Outline each Plasmodium falciparum-infected red blood cell.
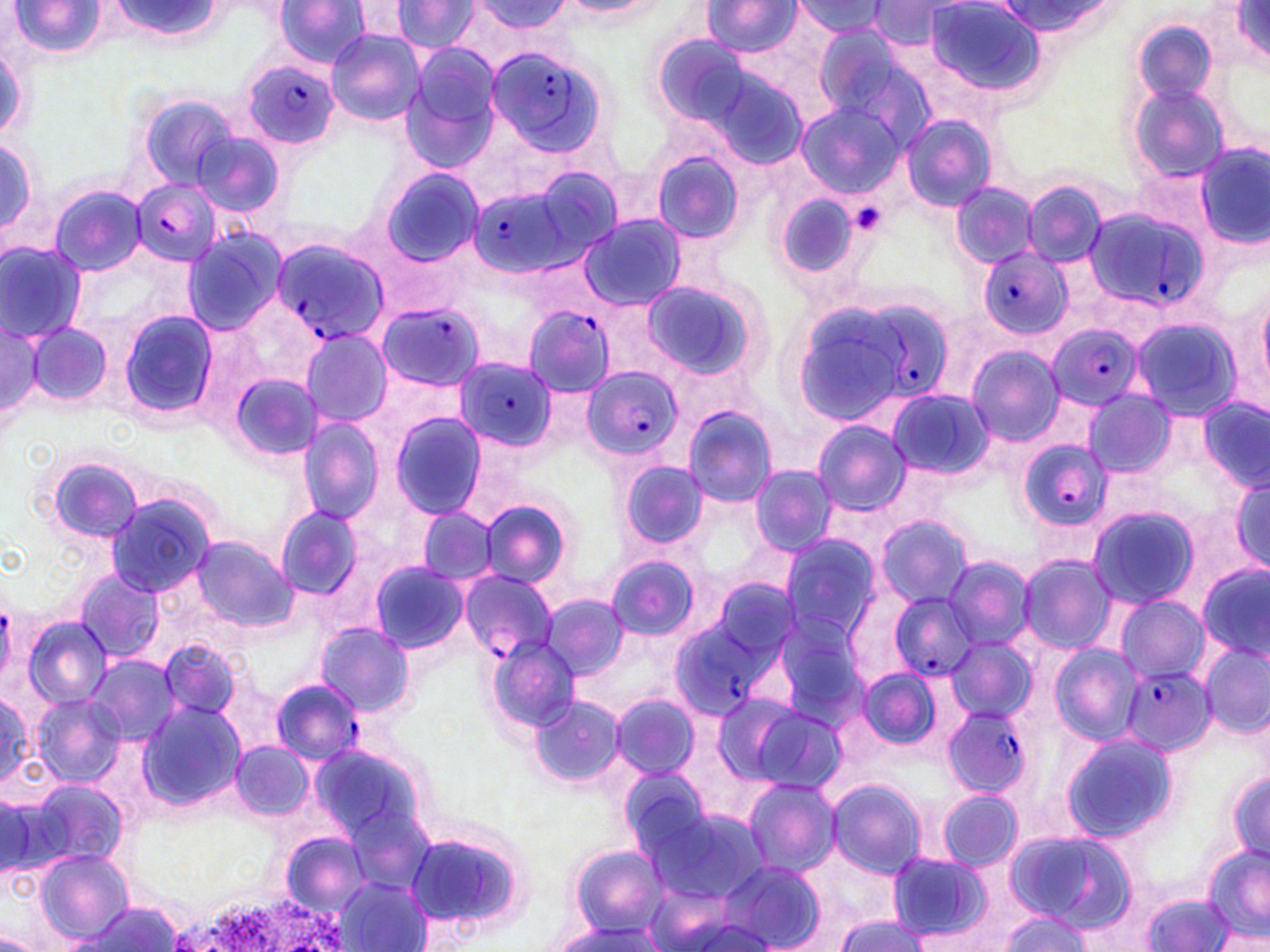

Approximate bounding boxes as (x1,y1)-(x2,y2) corner pairs in pixels.
Plasmodium falciparum-infected red blood cells: (483,40)-(618,158), (244,61)-(341,149), (131,180)-(221,265), (466,180)-(590,281), (1077,206)-(1210,317), (270,238)-(390,345), (979,248)-(1072,335), (853,296)-(949,397), (378,301)-(488,389), (523,306)-(616,395), (1044,323)-(1143,412), (455,357)-(557,451), (581,366)-(681,461), (1015,436)-(1107,537), (458,568)-(558,662), (887,591)-(982,681), (666,602)-(793,722), (1122,667)-(1215,754), (271,677)-(365,765), (944,705)-(1033,797).

Summary:
  - Uninfected red blood cell locations: (7,0)-(107,59), (273,1)-(374,68), (351,1)-(417,46), (391,1)-(483,55), (465,1)-(577,42), (558,1)-(667,21), (702,2)-(802,55), (792,2)-(892,38), (867,2)-(958,48), (924,2)-(1047,95), (1226,2)-(1270,67), (105,3)-(228,43), (987,3)-(1125,38), (1132,20)-(1219,109), (815,26)-(932,141), (324,28)-(424,125), (1,39)-(31,143), (401,46)-(503,170), (1126,81)-(1231,182), (134,93)-(242,191), (794,102)-(902,200), (901,114)-(996,213), (189,129)-(286,218), (0,134)-(43,251), (1191,146)-(1269,250), (648,150)-(748,244), (374,167)-(484,269), (950,182)-(1039,267), (1022,182)-(1108,268), (48,184)-(149,275), (774,192)-(864,282), (579,214)-(690,312), (180,227)-(288,336), (0,241)-(89,343), (639,276)-(770,384), (1256,281)-(1270,402), (117,309)-(219,421), (1127,315)-(1243,421), (1,318)-(43,427), (25,320)-(113,411), (298,328)-(392,427), (965,345)-(1064,447), (228,373)-(323,462), (886,387)-(993,480), (1082,391)-(1175,476), (1198,397)-(1269,491), (682,405)-(778,508), (387,411)-(488,520), (299,419)-(384,522), (812,420)-(911,517), (38,452)-(150,549), (619,459)-(710,549), (748,464)-(838,555), (1225,471)-(1270,579), (106,494)-(216,597), (475,497)-(576,593), (273,504)-(366,601), (1086,504)-(1202,609), (417,507)-(500,585), (875,515)-(975,609), (780,534)-(882,646), (191,537)-(295,630), (1017,554)-(1116,652), (604,555)-(700,641), (942,555)-(1036,651), (368,559)-(471,655), (1196,566)-(1269,660), (74,569)-(163,663), (540,596)-(629,681), (1115,596)-(1211,682), (767,613)-(869,726), (21,615)-(113,708), (315,623)-(414,717), (157,636)-(246,723), (486,636)-(579,732), (945,636)-(1035,721), (1049,643)-(1143,743), (1201,644)-(1268,737), (87,655)-(181,747), (853,667)-(947,752), (0,687)-(34,789), (30,693)-(124,787), (609,695)-(700,781), (530,696)-(626,787), (740,700)-(847,796), (139,701)-(244,811), (1058,731)-(1179,844), (232,741)-(311,820), (1226,764)-(1270,866), (618,765)-(718,863), (742,776)-(840,875), (825,777)-(926,879), (25,778)-(128,874), (935,788)-(1023,869), (2,795)-(52,877), (644,804)-(771,904), (400,822)-(535,937), (1002,830)-(1133,929), (283,834)-(368,911), (1200,843)-(1270,943), (567,845)-(671,938), (39,851)-(132,943), (885,852)-(992,942), (716,860)-(827,952), (335,876)-(433,952), (1140,891)-(1236,951), (73,902)-(186,950), (832,911)-(930,952), (995,911)-(1093,951), (546,918)-(668,952), (0,932)-(42,952)
  - Platelet locations: (845,201)-(888,236)
  - Slide-level diagnosis: Plasmodium falciparum
  - Magnification: 1000x
  - Preparation: thin blood smear
  - Image size: 1270×952 pixels
  - Modality: optical microscopy
  - Field of view: single
  - Stain: May-Grünwald-Giemsa